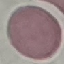
malaria status = uninfected
image type = cell patch, automatically extracted from a larger field of view and resized to 64 × 64 pixels
preparation = thin blood film
stain = Giemsa
capture = smartphone camera at the microscope eyepiece